Comment on the morphology of the red blood cells.
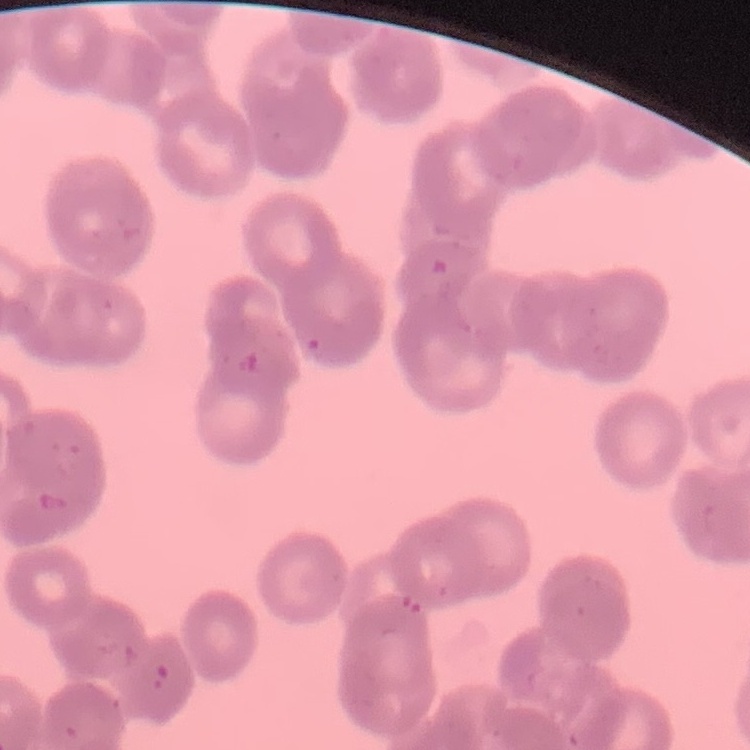
Rouleaux formation.

{
  "preparation": "thin peripheral smear",
  "stain": "Field's or Giemsa",
  "image_type": "square crop of a larger photomicrograph"
}